Assess this cell for malaria.
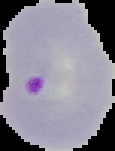
It is parasitized.

Summary:
  - Image type: segmented cell region with the area outside set to black
  - Preparation: thin blood film
  - Image size: 115×151 pixels